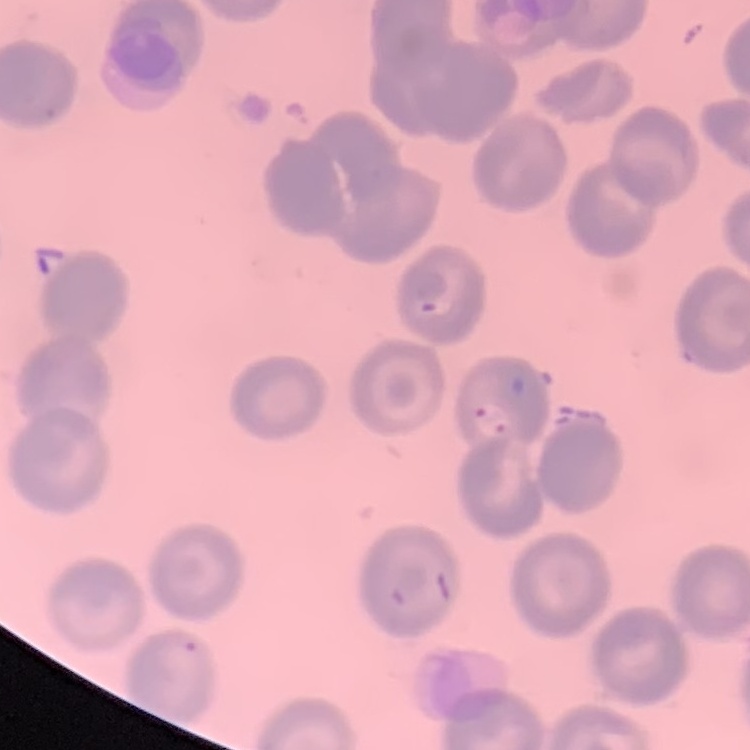
erythrocyte_morphology: no rouleaux formation
preparation: thin peripheral smear
image_type: square crop of a larger photomicrograph
stain: Field's or Giemsa